State which cell type is depicted.
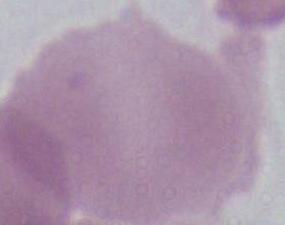
This is an erythrocyte.

Photomicrograph. Captured at 1000x magnification.